Name the blood parasite species.
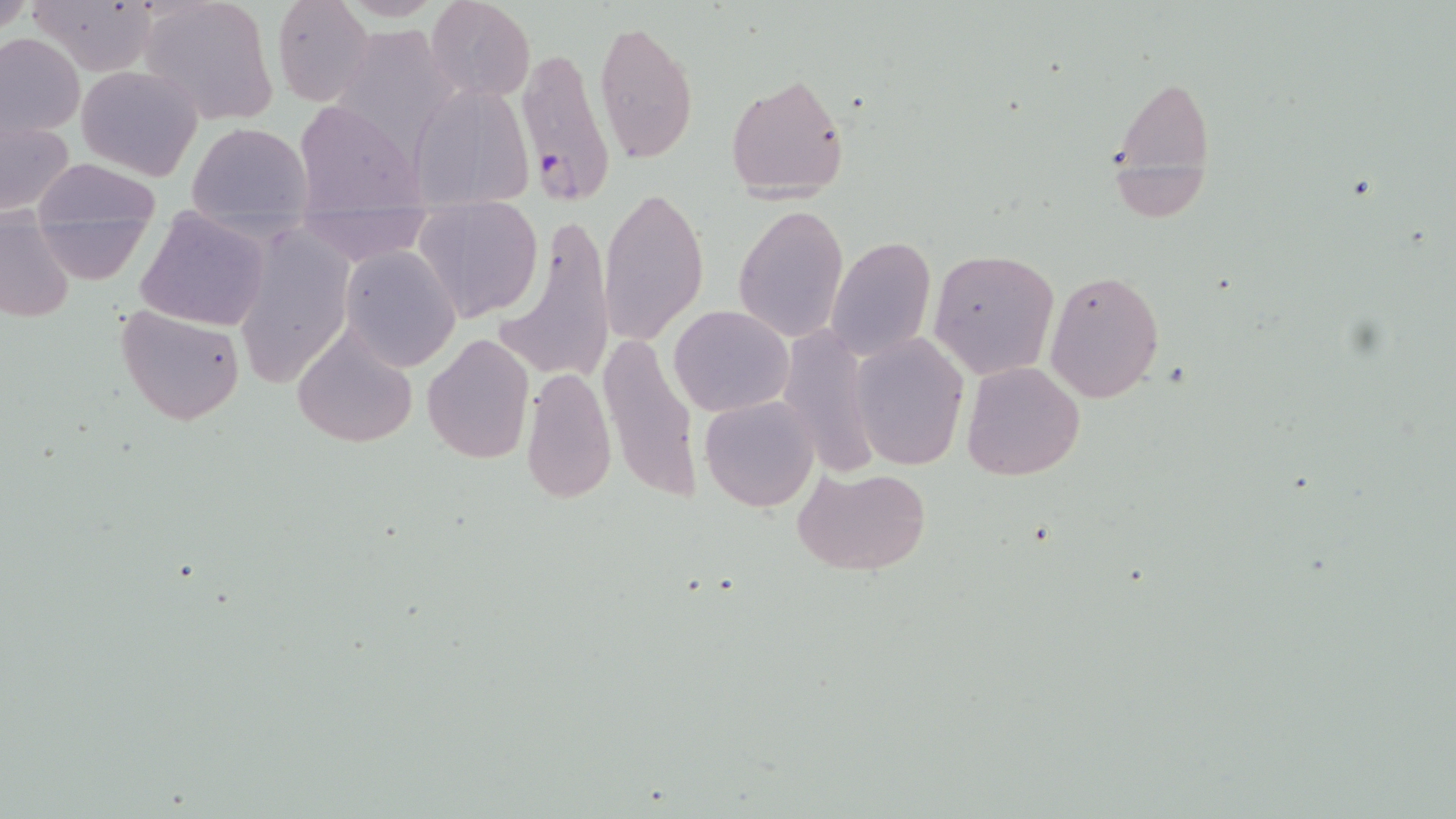
Plasmodium falciparum.

Summary:
  - Coordinate format: approximate bounding boxes as named x1/y1/x2/y2 corners in pixels
  - Uninfected red blood cell locations: (x1=138, y1=0, x2=278, y2=126), (x1=271, y1=0, x2=376, y2=107), (x1=425, y1=0, x2=535, y2=104), (x1=30, y1=1, x2=160, y2=74), (x1=593, y1=18, x2=698, y2=165), (x1=329, y1=25, x2=459, y2=153), (x1=0, y1=32, x2=84, y2=141), (x1=75, y1=64, x2=205, y2=182), (x1=726, y1=73, x2=850, y2=200), (x1=1109, y1=74, x2=1215, y2=215), (x1=411, y1=83, x2=532, y2=207), (x1=293, y1=99, x2=425, y2=213), (x1=1, y1=118, x2=76, y2=216), (x1=186, y1=121, x2=311, y2=232), (x1=29, y1=158, x2=160, y2=268), (x1=599, y1=189, x2=707, y2=349), (x1=413, y1=199, x2=543, y2=322), (x1=734, y1=204, x2=849, y2=343), (x1=136, y1=206, x2=271, y2=331), (x1=295, y1=206, x2=431, y2=267), (x1=1, y1=214, x2=74, y2=323), (x1=498, y1=215, x2=612, y2=385), (x1=231, y1=226, x2=353, y2=384), (x1=826, y1=236, x2=937, y2=361), (x1=340, y1=245, x2=461, y2=370), (x1=928, y1=249, x2=1059, y2=378), (x1=1044, y1=269, x2=1165, y2=403), (x1=115, y1=304, x2=246, y2=426), (x1=669, y1=304, x2=795, y2=418), (x1=289, y1=326, x2=418, y2=450), (x1=775, y1=327, x2=881, y2=474), (x1=596, y1=330, x2=700, y2=507), (x1=850, y1=331, x2=968, y2=470), (x1=422, y1=332, x2=535, y2=465), (x1=961, y1=361, x2=1086, y2=481), (x1=520, y1=365, x2=616, y2=506), (x1=700, y1=394, x2=819, y2=512), (x1=795, y1=465, x2=932, y2=575)
  - Plasmodium falciparum-infected red blood cell locations: (x1=515, y1=46, x2=615, y2=207)
  - Field of view: one of a larger specimen
  - Magnification: 1000x
  - Modality: optical microscopy
  - Stain: May-Grünwald-Giemsa
  - Preparation: thin blood film
  - Image size: 1456×819 pixels